Comment on the morphology of the erythrocytes.
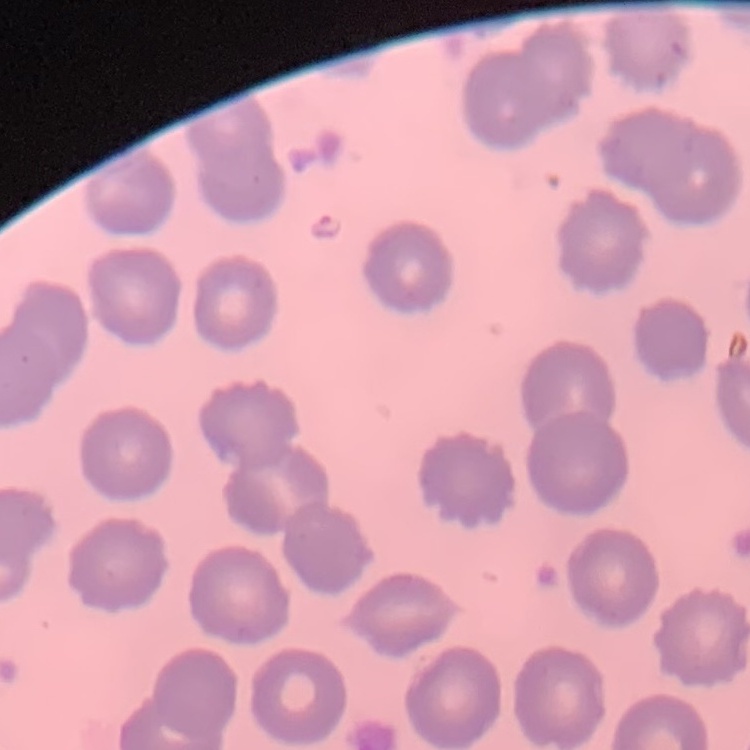
They show no rouleaux formation.

stain = Field's or Giemsa
preparation = thin blood film
image type = one tile cut from a larger photomicrograph